State the blood parasite species.
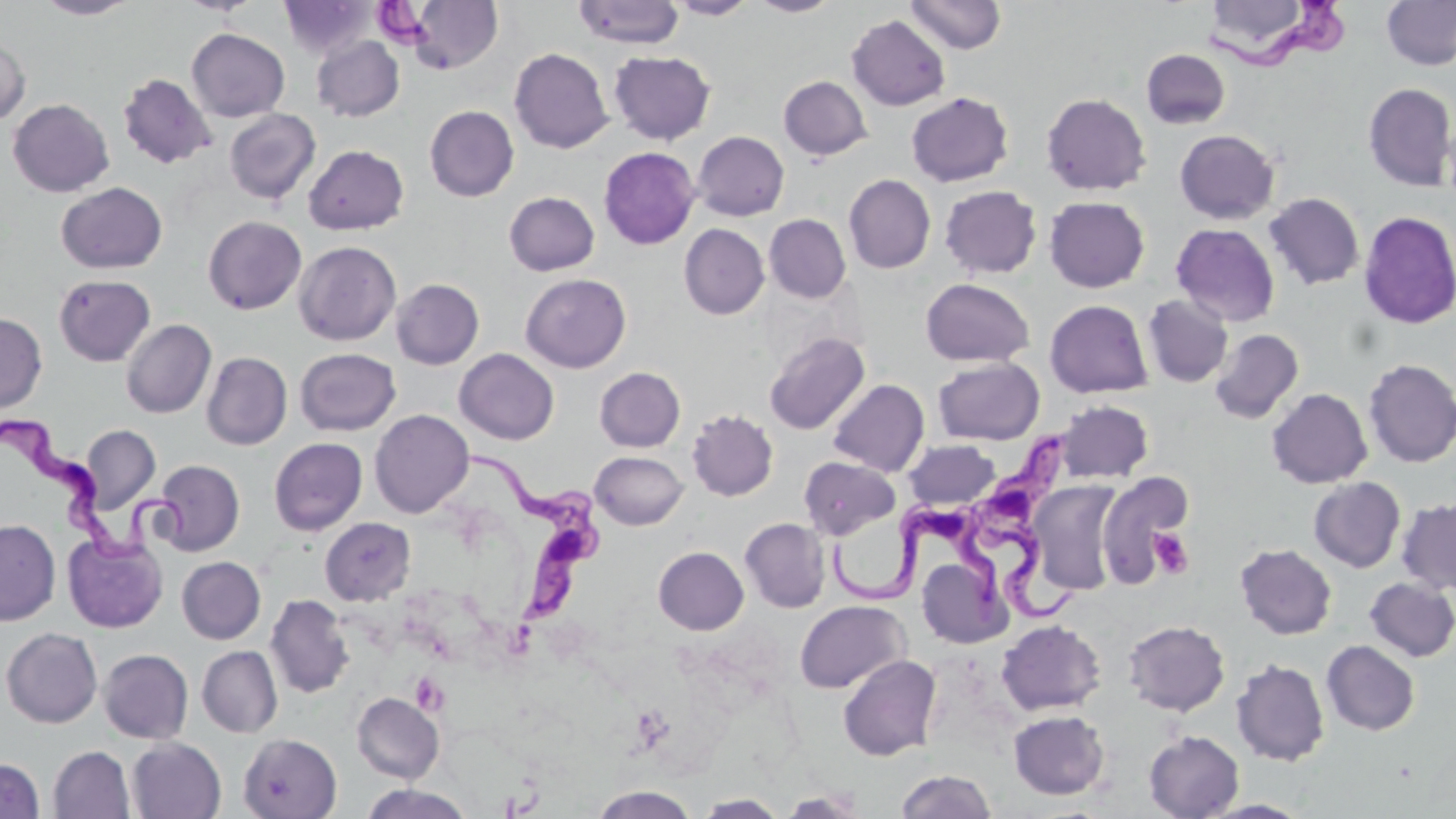

Trypanosoma brucei.

{
  "uninfected_red_blood_cell_locations": "approximate bounding boxes as [x1, y1, x2, y2] in pixels: [34, 0, 141, 19], [176, 0, 264, 15], [278, 0, 376, 59], [664, 0, 759, 19], [750, 0, 840, 16], [906, 0, 1007, 54], [1382, 0, 1456, 70], [406, 1, 503, 74], [573, 1, 685, 48], [1203, 1, 1316, 65], [847, 15, 950, 111], [187, 28, 290, 122], [0, 33, 31, 126], [312, 36, 405, 122], [509, 48, 613, 153], [1141, 49, 1230, 129], [608, 50, 716, 145], [117, 73, 216, 169], [779, 76, 872, 160], [1363, 82, 1456, 191], [905, 91, 1014, 187], [1040, 93, 1152, 196], [7, 98, 114, 197], [425, 105, 519, 201], [224, 108, 320, 204], [1174, 129, 1280, 224], [693, 131, 789, 220], [304, 144, 409, 235], [598, 146, 700, 249], [844, 174, 936, 273], [56, 182, 167, 274], [939, 185, 1042, 279], [504, 191, 600, 276], [1264, 192, 1364, 290], [1044, 196, 1150, 292], [1358, 210, 1456, 329], [764, 214, 851, 303], [202, 216, 307, 314], [1172, 223, 1280, 326], [679, 224, 769, 320], [294, 241, 401, 345], [521, 273, 631, 373], [54, 274, 155, 366], [391, 278, 484, 369], [920, 278, 1034, 367], [1142, 294, 1233, 388], [1044, 299, 1153, 398], [0, 312, 47, 413], [121, 319, 216, 418], [1210, 329, 1304, 424], [763, 332, 870, 435], [295, 348, 401, 436], [455, 348, 559, 445], [201, 352, 292, 450], [933, 356, 1044, 445], [1362, 358, 1456, 468], [594, 367, 685, 452], [828, 379, 929, 477], [1267, 388, 1372, 488], [1055, 400, 1153, 483], [369, 409, 474, 518], [687, 409, 778, 501], [81, 425, 161, 514], [269, 437, 367, 535], [904, 440, 1001, 510], [590, 451, 688, 530], [798, 456, 899, 539], [151, 459, 245, 556], [1096, 472, 1192, 586], [1308, 477, 1406, 572], [1027, 481, 1123, 595], [1397, 498, 1456, 596], [320, 517, 415, 605], [740, 517, 830, 613], [0, 519, 60, 626], [62, 532, 168, 633], [1235, 543, 1337, 640], [654, 546, 749, 635], [177, 556, 266, 644], [916, 556, 1012, 648], [1364, 577, 1456, 661], [265, 594, 354, 698], [795, 600, 910, 693], [996, 619, 1106, 715], [1123, 620, 1229, 716], [0, 627, 103, 728], [1321, 640, 1420, 735], [197, 646, 283, 737], [99, 649, 194, 744], [838, 654, 942, 761], [1231, 658, 1330, 766], [352, 692, 444, 783], [1009, 710, 1109, 799], [1143, 731, 1244, 819], [238, 733, 343, 818], [127, 738, 226, 819], [48, 746, 135, 819], [0, 758, 45, 818], [896, 770, 997, 818], [360, 784, 475, 819], [588, 786, 699, 818], [776, 789, 870, 818], [694, 793, 788, 818], [1200, 799, 1313, 818]",
  "magnification": "1000x",
  "preparation": "thin blood film",
  "stain": "May-Grünwald-Giemsa",
  "field_of_view": "one of a larger specimen",
  "modality": "optical microscopy",
  "platelet_locations": "approximate bounding boxes as [x1, y1, x2, y2] in pixels: [373, 3, 430, 47], [1147, 528, 1193, 579], [410, 673, 449, 715]",
  "image_size": "1456×819 pixels",
  "trypanosoma_brucei_locations": "approximate bounding boxes as [x1, y1, x2, y2] in pixels: [1211, 0, 1350, 72], [0, 413, 189, 565], [972, 428, 1082, 624], [467, 455, 605, 631], [827, 510, 1009, 613]"
}